Assess the morphology of the red blood cells.
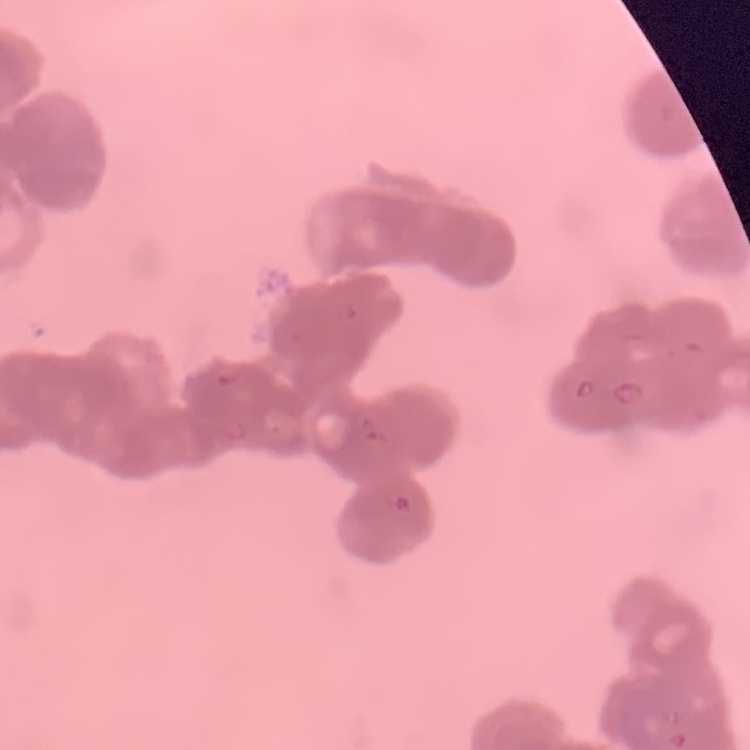

They show rouleaux formation.

stain = Field's or Giemsa
preparation = thin peripheral smear
image type = square crop of a larger photomicrograph